Report the malaria status of this cell.
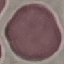
It is uninfected.

Summary:
  - Stain: Giemsa
  - Preparation: thin blood film
  - Image type: automatically extracted cell patch, resized to 64 × 64 pixels
  - Capture: smartphone camera at the microscope eyepiece